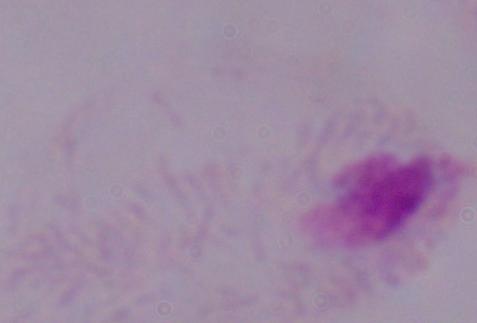
Summary:
  - Modality: photomicrograph
  - Identification: trichomonad
  - Magnification: 1000x